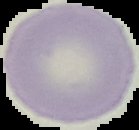
Segmented cell region on a black background. From a thin blood film. Result: negative for malaria parasites. Image is 139×130 pixels.